State which parasite is depicted.
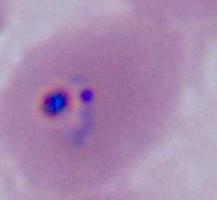
This is Plasmodium.

modality = micrograph
magnification = 400x or 1000x